Assess this cell for malaria.
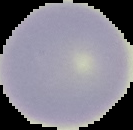
Uninfected.

From a thin blood smear. Image is 133×130 pixels. Cell region segmented out of the field of view; the surrounding area is masked to black.